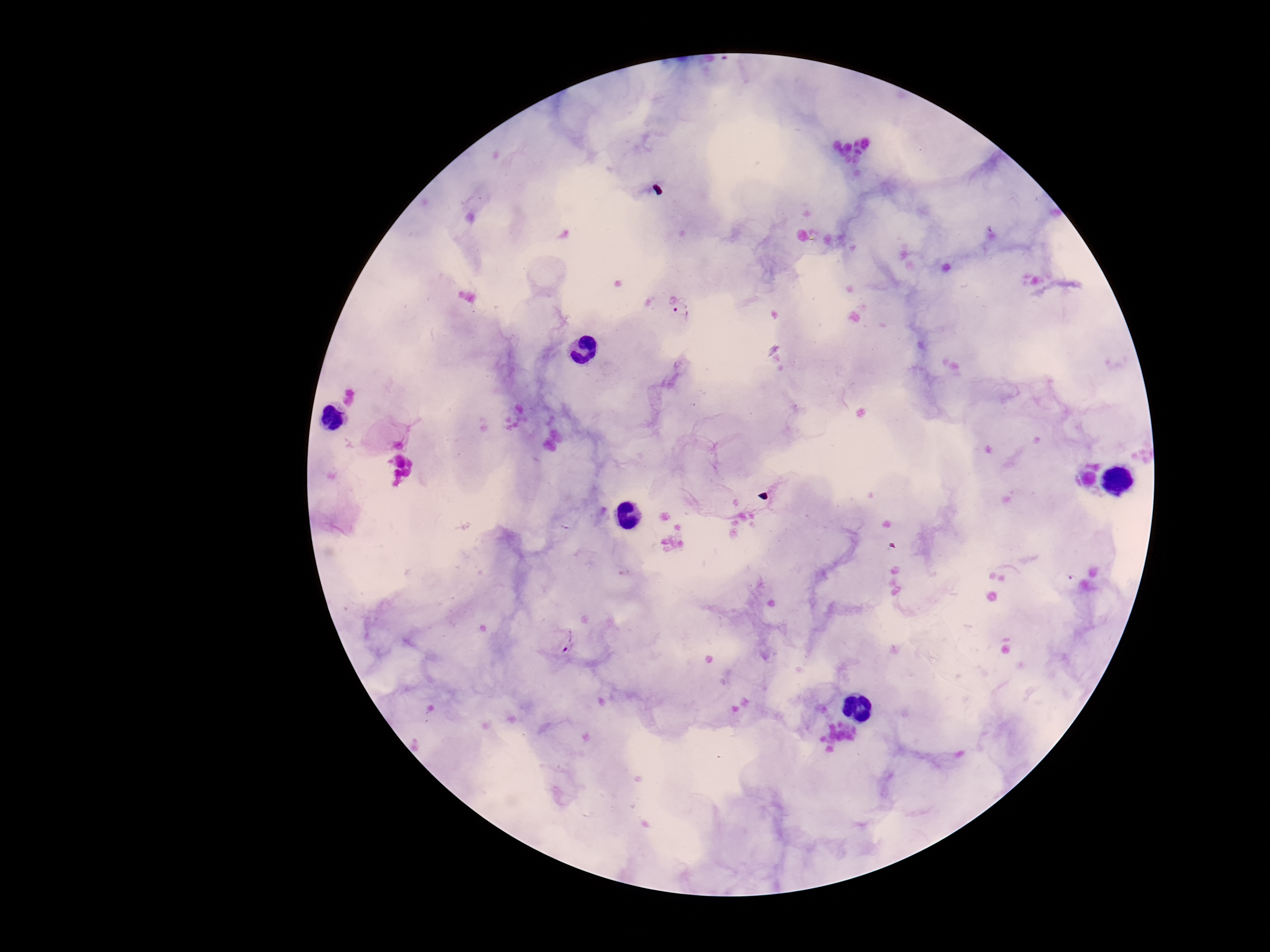
{
  "patient_malaria_status": "positive",
  "field_of_view": "one from this slide",
  "magnification": "100x",
  "plasmodium_parasite_locations": "approximate centers as (x, y) in pixels: (682, 312), (569, 641)",
  "preparation": "thick blood film",
  "capture": "smartphone camera through the microscope eyepiece",
  "stain": "Giemsa",
  "image_size": "1270×952 pixels"
}